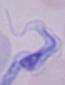

Summary:
  - Modality: micrograph
  - Magnification: 1000x
  - Identification: trypanosome